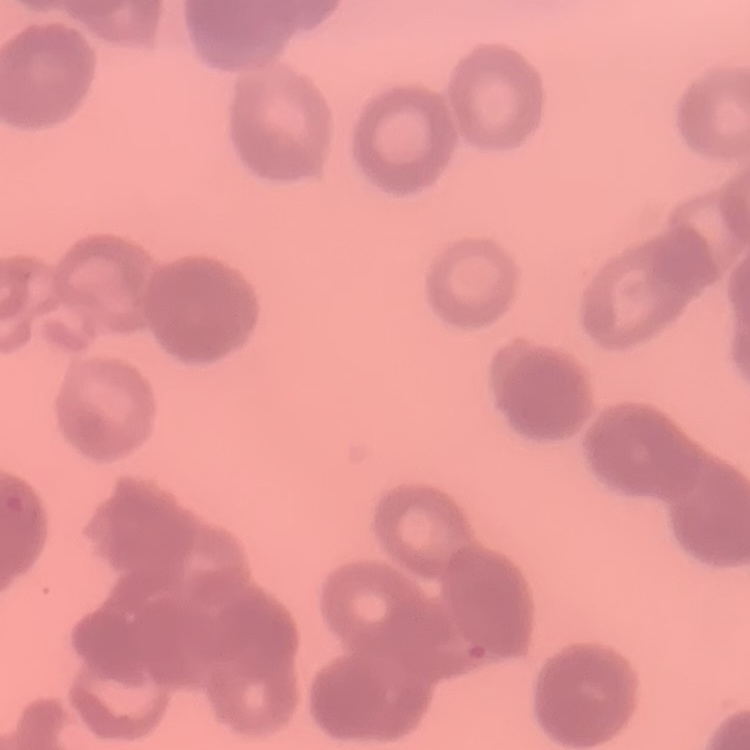

Summary:
  - Erythrocyte morphology: rouleaux formation
  - Preparation: thin peripheral smear
  - Image type: one tile cut from a larger photomicrograph
  - Stain: Field's or Giemsa